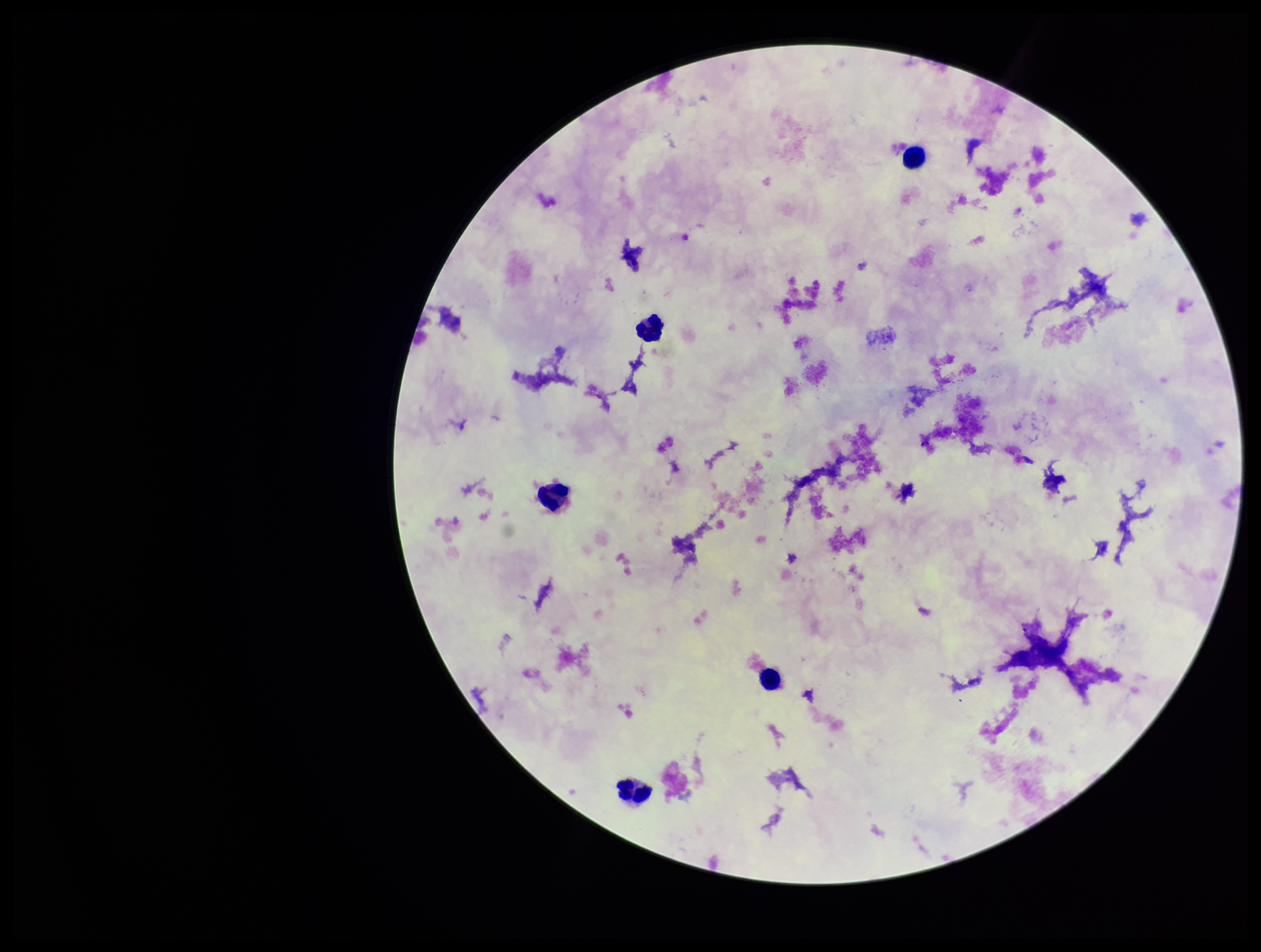

Single field of view. Leukocyte count: 5. Plasmodium parasites: none detected. Smartphone photograph taken through the eyepiece of a microscope. Giemsa stain. Parasite count: 0. Preparation: thick. Image is 1261×952 pixels. Patient malaria status: negative.